State the blood parasite species.
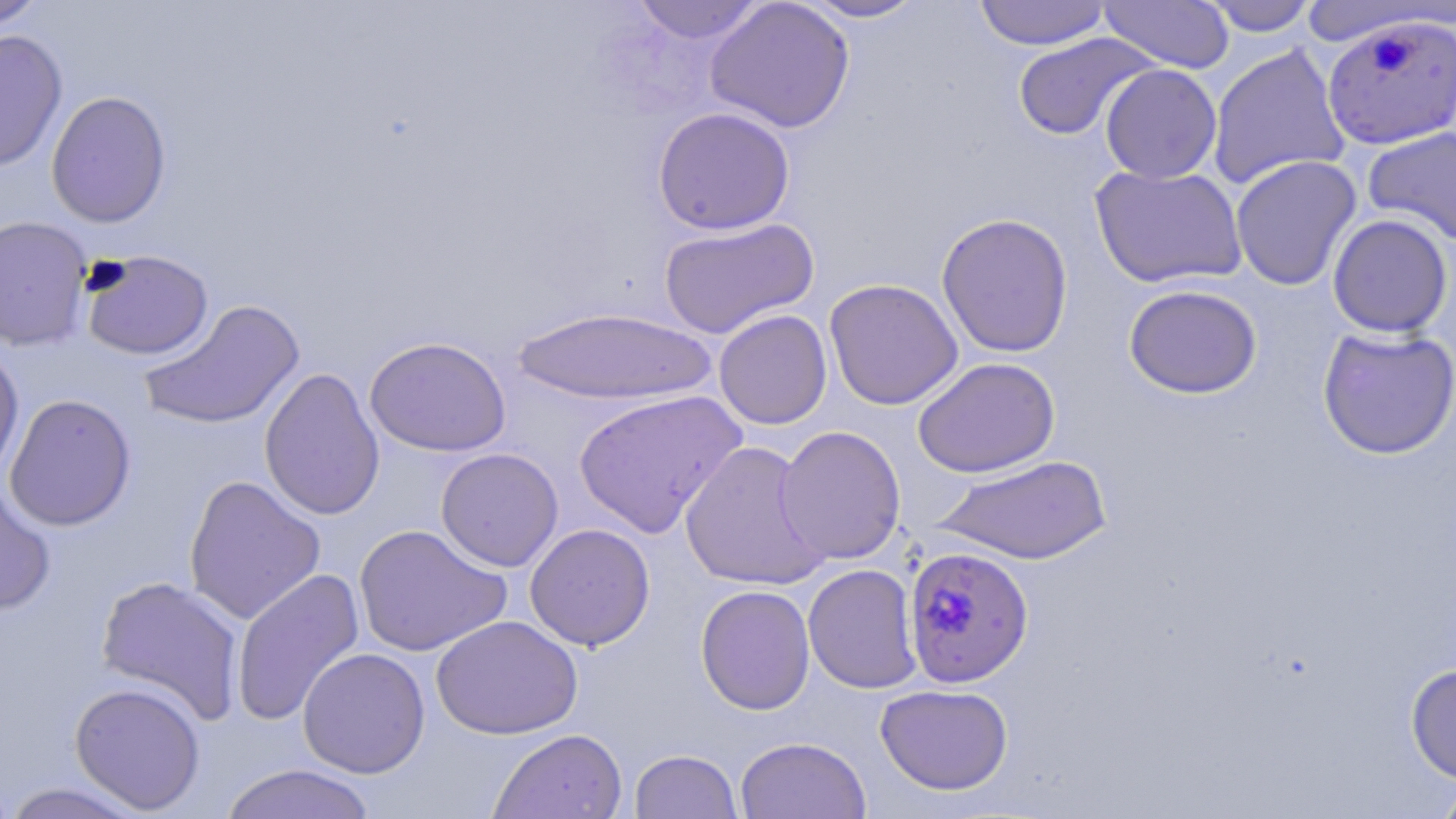

Plasmodium falciparum.

Summary:
  - Coordinate format: approximate bounding boxes as (x1,y1)-(x2,y2) corner pairs in pixels
  - Uninfected red blood cell locations: (0,0)-(49,32), (630,0)-(767,44), (704,0)-(856,134), (796,0)-(929,22), (973,0)-(1111,50), (1198,0)-(1320,36), (1099,1)-(1234,73), (1296,2)-(1453,47), (0,29)-(68,172), (1012,32)-(1158,141), (1207,43)-(1351,190), (1100,64)-(1222,184), (46,90)-(172,228), (652,107)-(795,235), (1362,127)-(1456,246), (1230,154)-(1362,291), (1090,163)-(1247,289), (936,212)-(1074,357), (1327,214)-(1453,338), (0,216)-(94,352), (658,217)-(819,339), (80,250)-(214,361), (824,278)-(963,410), (1124,284)-(1262,399), (140,300)-(305,430), (511,307)-(718,406), (713,309)-(833,430), (1317,326)-(1456,459), (364,335)-(512,458), (0,342)-(24,483), (912,357)-(1060,478), (259,367)-(386,521), (572,389)-(747,538), (4,393)-(137,531), (776,425)-(907,565), (679,440)-(829,591), (435,447)-(564,571), (934,454)-(1111,565), (184,475)-(326,625), (0,480)-(57,615), (354,523)-(511,658), (525,523)-(655,650), (803,563)-(922,694), (231,568)-(365,727), (95,575)-(246,724), (695,584)-(815,715), (431,615)-(583,740), (297,647)-(430,778), (1406,663)-(1456,784), (69,681)-(207,814), (875,684)-(1013,795), (488,728)-(628,819), (735,736)-(871,819), (630,749)-(742,819), (218,763)-(379,819), (0,771)-(18,819), (1431,777)-(1456,819), (0,781)-(152,818)
  - Plasmodium falciparum-infected red blood cell locations: (1322,14)-(1456,151), (903,546)-(1034,688)
  - Image size: 1456×819 pixels
  - Field of view: one of a larger specimen
  - Modality: optical microscopy
  - Preparation: thin blood smear
  - Magnification: 1000x
  - Stain: May-Grünwald-Giemsa